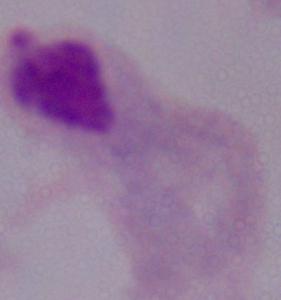
Summary:
  - Modality: micrograph
  - Magnification: 1000x
  - Identification: trichomonad